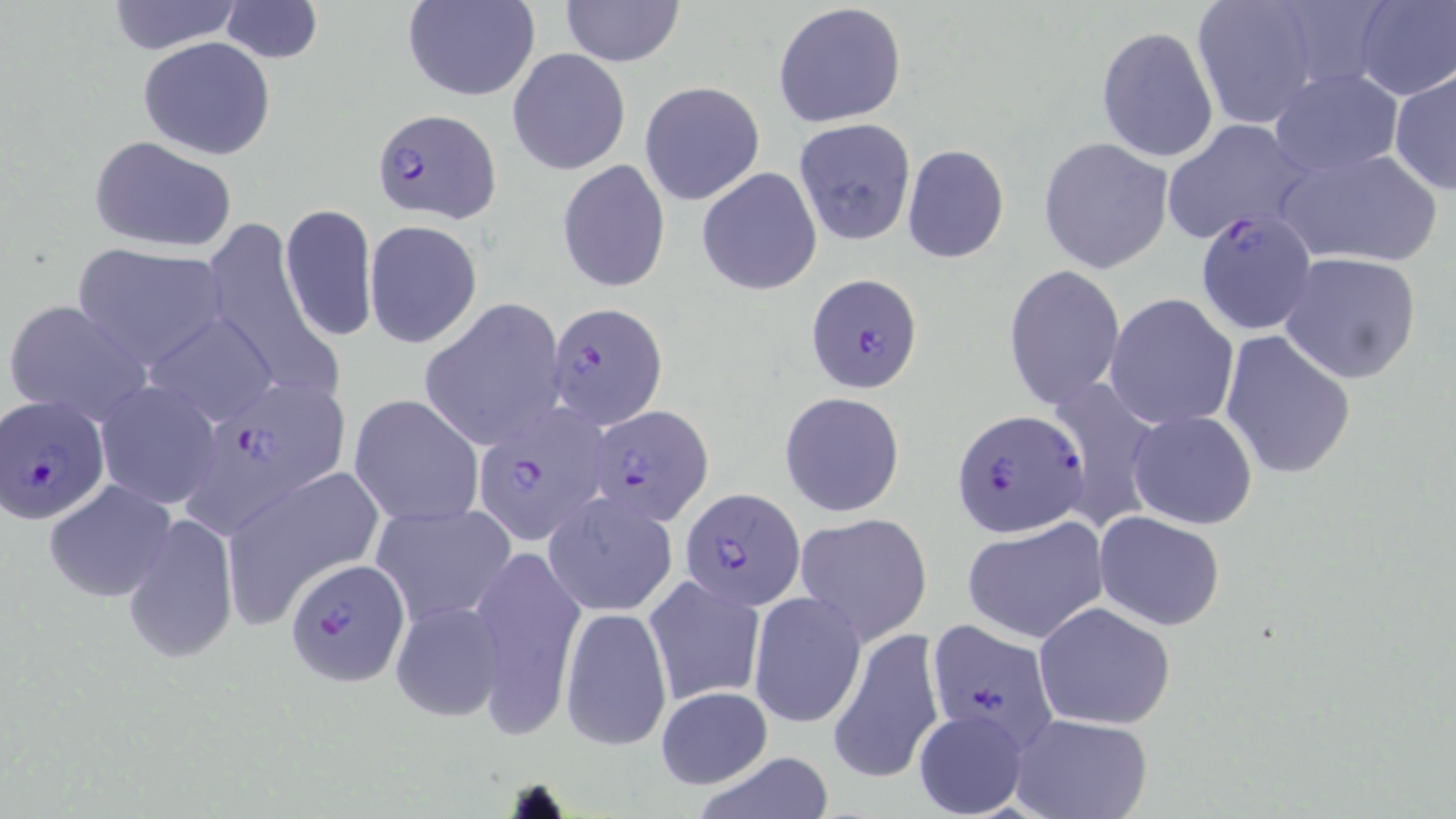

Approximate bounding boxes as named x1/y1/x2/y2 corners in pixels. Uninfected red blood cell locations: (x1=103, y1=0, x2=246, y2=54), (x1=403, y1=0, x2=540, y2=101), (x1=559, y1=0, x2=686, y2=67), (x1=1187, y1=0, x2=1324, y2=128), (x1=1352, y1=0, x2=1455, y2=100), (x1=219, y1=1, x2=323, y2=63), (x1=773, y1=2, x2=907, y2=128), (x1=1095, y1=26, x2=1219, y2=163), (x1=137, y1=36, x2=277, y2=159), (x1=507, y1=48, x2=630, y2=176), (x1=1388, y1=66, x2=1455, y2=196), (x1=1267, y1=68, x2=1405, y2=178), (x1=639, y1=80, x2=765, y2=205), (x1=1162, y1=118, x2=1312, y2=245), (x1=793, y1=119, x2=918, y2=247), (x1=87, y1=135, x2=237, y2=253), (x1=1039, y1=137, x2=1173, y2=273), (x1=902, y1=143, x2=1008, y2=264), (x1=1276, y1=146, x2=1444, y2=269), (x1=558, y1=159, x2=671, y2=293), (x1=697, y1=167, x2=823, y2=296), (x1=279, y1=204, x2=377, y2=343), (x1=364, y1=221, x2=482, y2=348), (x1=203, y1=222, x2=339, y2=405), (x1=71, y1=243, x2=231, y2=368), (x1=1278, y1=251, x2=1424, y2=383), (x1=1003, y1=265, x2=1125, y2=410), (x1=1105, y1=293, x2=1240, y2=430), (x1=4, y1=299, x2=152, y2=426), (x1=421, y1=299, x2=566, y2=450), (x1=140, y1=311, x2=280, y2=427), (x1=1219, y1=329, x2=1355, y2=480), (x1=1045, y1=377, x2=1159, y2=536), (x1=96, y1=381, x2=222, y2=509), (x1=779, y1=391, x2=905, y2=518), (x1=350, y1=395, x2=482, y2=528), (x1=1127, y1=409, x2=1259, y2=529), (x1=218, y1=465, x2=382, y2=617), (x1=45, y1=479, x2=175, y2=600), (x1=543, y1=492, x2=678, y2=617), (x1=371, y1=500, x2=517, y2=627), (x1=1094, y1=511, x2=1225, y2=629), (x1=796, y1=512, x2=932, y2=644), (x1=121, y1=513, x2=240, y2=665), (x1=962, y1=518, x2=1109, y2=645), (x1=467, y1=547, x2=585, y2=730), (x1=644, y1=573, x2=766, y2=707), (x1=749, y1=591, x2=865, y2=729), (x1=390, y1=600, x2=506, y2=723), (x1=1033, y1=601, x2=1176, y2=730), (x1=560, y1=605, x2=672, y2=752), (x1=828, y1=627, x2=944, y2=786), (x1=655, y1=686, x2=774, y2=788), (x1=914, y1=708, x2=1029, y2=818), (x1=1010, y1=713, x2=1154, y2=819), (x1=689, y1=750, x2=839, y2=819). Plasmodium falciparum-infected red blood cell locations: (x1=375, y1=109, x2=504, y2=223), (x1=1195, y1=210, x2=1317, y2=339), (x1=804, y1=271, x2=923, y2=393), (x1=546, y1=300, x2=668, y2=428), (x1=184, y1=379, x2=352, y2=524), (x1=1, y1=397, x2=110, y2=525), (x1=584, y1=403, x2=713, y2=525), (x1=473, y1=404, x2=611, y2=544), (x1=956, y1=406, x2=1089, y2=539), (x1=680, y1=487, x2=805, y2=608), (x1=283, y1=557, x2=411, y2=688), (x1=923, y1=619, x2=1060, y2=753). Slide-level diagnosis: Plasmodium falciparum. May-Grünwald-Giemsa-stained preparation. 1000x magnification. Thin blood smear. Image is 1456×819 pixels. Light microscopy. Single field of view.